Assess this cell for malaria.
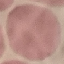

Uninfected.

image type = cell patch, automatically extracted from a larger field of view and resized to 64 × 64 pixels
preparation = thin blood smear
stain = Giemsa
capture = smartphone through the microscope eyepiece